Evaluate for malaria.
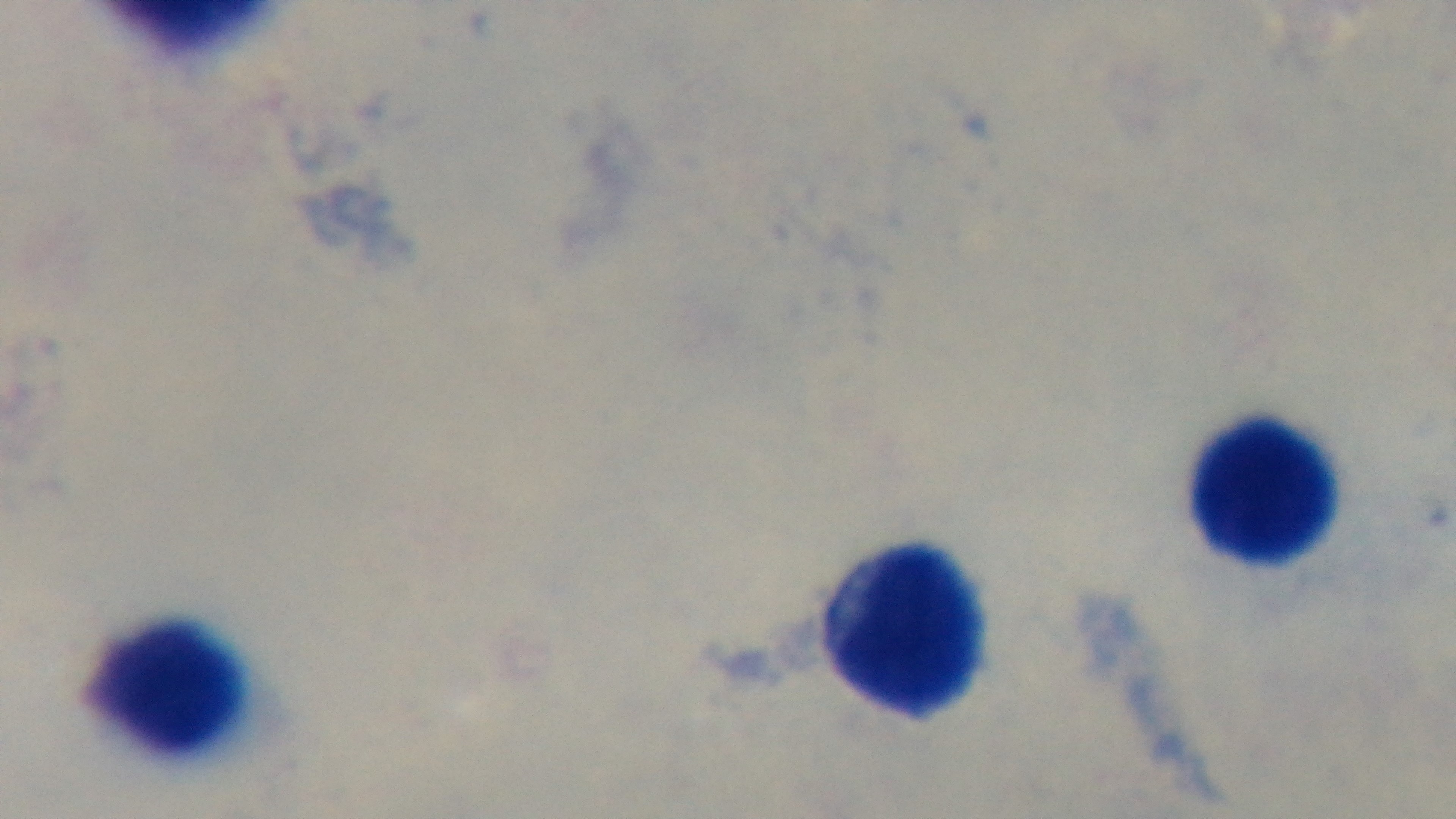

It is uninfected.

Photomicrograph. 100x oil-immersion objective. Preparation: thick. Giemsa-stained. Single field of view. Mounted 4K digital camera.